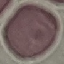

Summary:
  - Malaria status: uninfected
  - Image type: cell patch, automatically extracted from a larger field of view and resized to 64 × 64 pixels
  - Capture: smartphone through the microscope eyepiece
  - Preparation: thin smear
  - Stain: Giemsa